Report the malaria status of this cell.
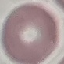
Uninfected.

Summary:
  - Image type: automatically extracted cell patch, resized to 64 × 64 pixels
  - Preparation: thin blood film
  - Stain: Giemsa
  - Capture: smartphone through the microscope eyepiece